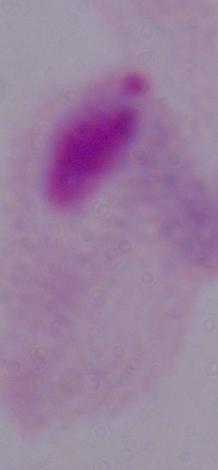

1000x magnification. Photomicrograph. A trichomonad is shown.